Outline each white blood cell.
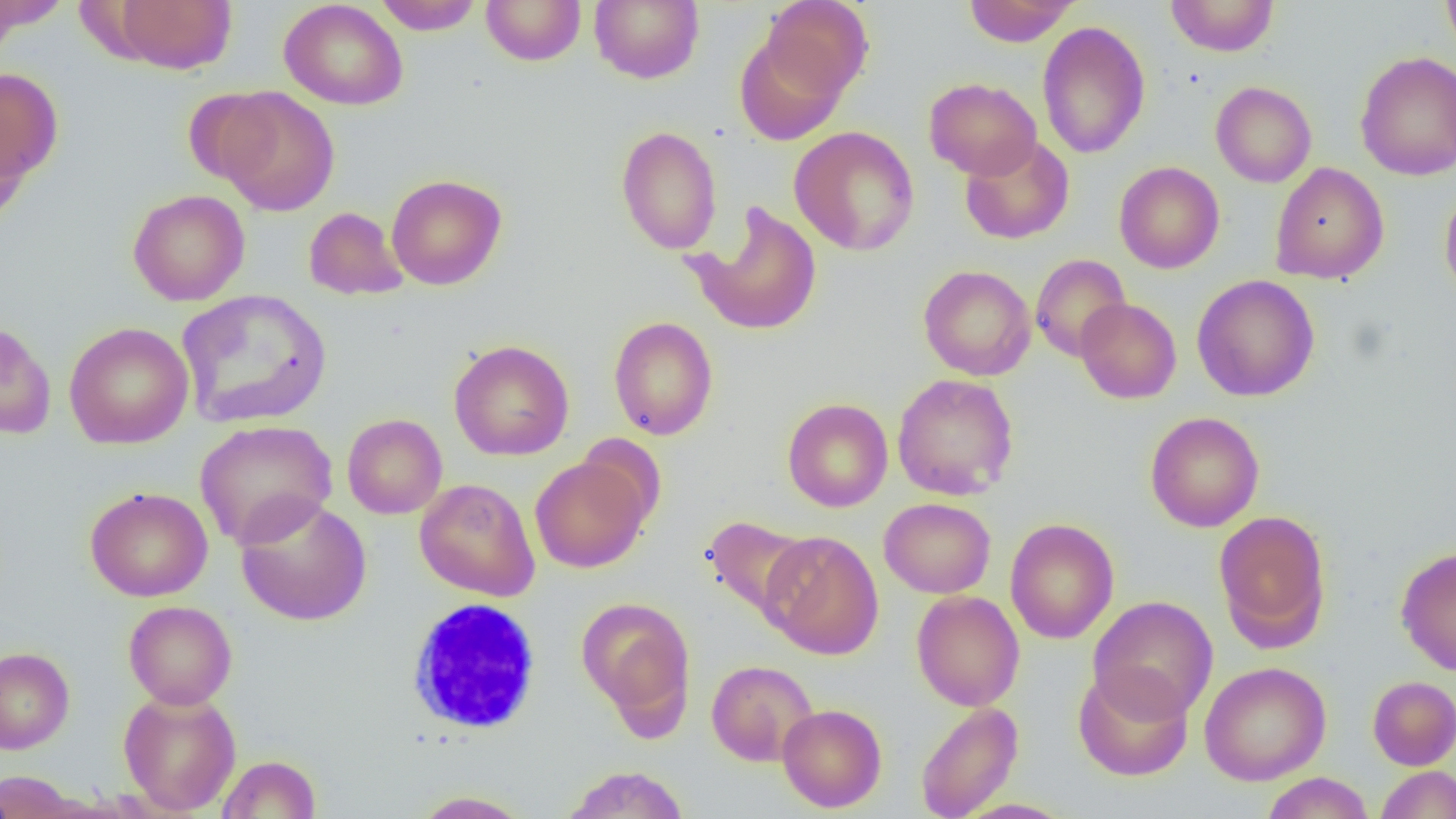

Approximate bounding boxes as named x1/y1/x2/y2 corners in pixels.
White blood cells: (x1=405, y1=597, x2=543, y2=736).

Uninfected red blood cell locations: (x1=111, y1=0, x2=237, y2=75), (x1=372, y1=0, x2=485, y2=35), (x1=480, y1=0, x2=587, y2=66), (x1=589, y1=0, x2=704, y2=84), (x1=761, y1=0, x2=874, y2=100), (x1=963, y1=0, x2=1080, y2=47), (x1=1165, y1=0, x2=1279, y2=57), (x1=1441, y1=0, x2=1456, y2=60), (x1=0, y1=1, x2=72, y2=35), (x1=279, y1=1, x2=408, y2=111), (x1=1036, y1=21, x2=1151, y2=158), (x1=734, y1=33, x2=847, y2=145), (x1=1355, y1=51, x2=1456, y2=180), (x1=0, y1=67, x2=64, y2=184), (x1=924, y1=77, x2=1041, y2=180), (x1=1210, y1=81, x2=1317, y2=187), (x1=215, y1=87, x2=340, y2=217), (x1=183, y1=89, x2=283, y2=186), (x1=0, y1=114, x2=32, y2=230), (x1=615, y1=125, x2=722, y2=255), (x1=789, y1=126, x2=920, y2=256), (x1=959, y1=135, x2=1074, y2=245), (x1=1113, y1=161, x2=1225, y2=274), (x1=1270, y1=162, x2=1388, y2=284), (x1=386, y1=173, x2=507, y2=290), (x1=1439, y1=184, x2=1456, y2=304), (x1=127, y1=189, x2=250, y2=306), (x1=687, y1=201, x2=824, y2=337), (x1=304, y1=206, x2=409, y2=300), (x1=1030, y1=254, x2=1131, y2=362), (x1=918, y1=265, x2=1036, y2=381), (x1=1191, y1=274, x2=1320, y2=401), (x1=177, y1=289, x2=332, y2=429), (x1=1075, y1=297, x2=1182, y2=403), (x1=608, y1=316, x2=719, y2=440), (x1=0, y1=319, x2=56, y2=439), (x1=64, y1=322, x2=194, y2=450), (x1=449, y1=339, x2=575, y2=461), (x1=892, y1=373, x2=1019, y2=500), (x1=782, y1=397, x2=893, y2=512), (x1=1144, y1=411, x2=1264, y2=532), (x1=342, y1=413, x2=447, y2=519), (x1=195, y1=419, x2=338, y2=549), (x1=575, y1=433, x2=666, y2=530), (x1=530, y1=455, x2=651, y2=573), (x1=414, y1=478, x2=540, y2=601), (x1=85, y1=486, x2=213, y2=602), (x1=234, y1=496, x2=373, y2=626), (x1=879, y1=497, x2=996, y2=598), (x1=1213, y1=509, x2=1332, y2=650), (x1=702, y1=515, x2=814, y2=624), (x1=1005, y1=518, x2=1120, y2=644), (x1=760, y1=530, x2=884, y2=659), (x1=1395, y1=545, x2=1456, y2=676), (x1=911, y1=590, x2=1025, y2=711), (x1=1089, y1=595, x2=1218, y2=722), (x1=575, y1=596, x2=696, y2=728), (x1=123, y1=600, x2=237, y2=709), (x1=0, y1=647, x2=75, y2=754), (x1=706, y1=660, x2=818, y2=766), (x1=1199, y1=661, x2=1331, y2=785), (x1=1072, y1=667, x2=1194, y2=781), (x1=1368, y1=675, x2=1456, y2=770), (x1=118, y1=688, x2=241, y2=816), (x1=915, y1=702, x2=1023, y2=819), (x1=777, y1=704, x2=887, y2=812), (x1=217, y1=755, x2=321, y2=818), (x1=559, y1=765, x2=690, y2=819), (x1=1375, y1=765, x2=1456, y2=818), (x1=0, y1=770, x2=83, y2=818), (x1=1261, y1=772, x2=1374, y2=819), (x1=412, y1=790, x2=534, y2=818). Slide-level diagnosis: negative for blood parasites. Image is 1456×819 pixels. 1000x magnification. Optical microscopy. Single field of view. Thin blood film.